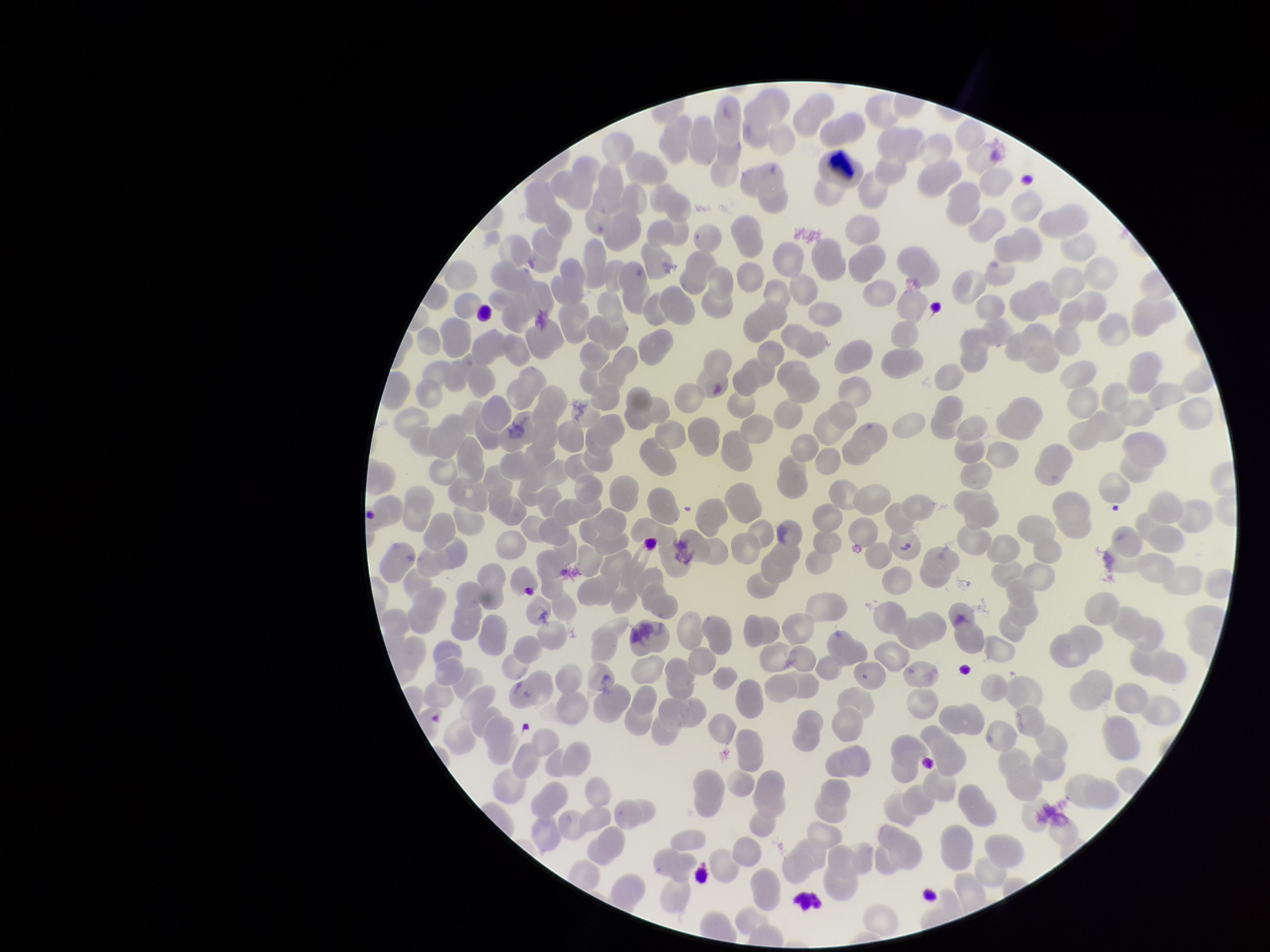
preparation: thin smear
species_reported_for_this_patient: Plasmodium falciparum
stain: Giemsa
patient_malaria_status: positive
image_size: 1270×952 pixels
red_blood_cell_count: 270
parasitized_red_blood_cells: none identified
parasitized_red_blood_cell_count: 0
field_of_view: one from this slide
capture: smartphone photograph through the microscope eyepiece